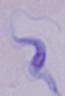
identification: trypanosome
modality: photomicrograph
magnification: 1000x